Assess this cell for malaria.
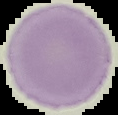
It is uninfected.

image size = 118×115 pixels
preparation = thin blood film
image type = segmented cell region with the area outside set to black